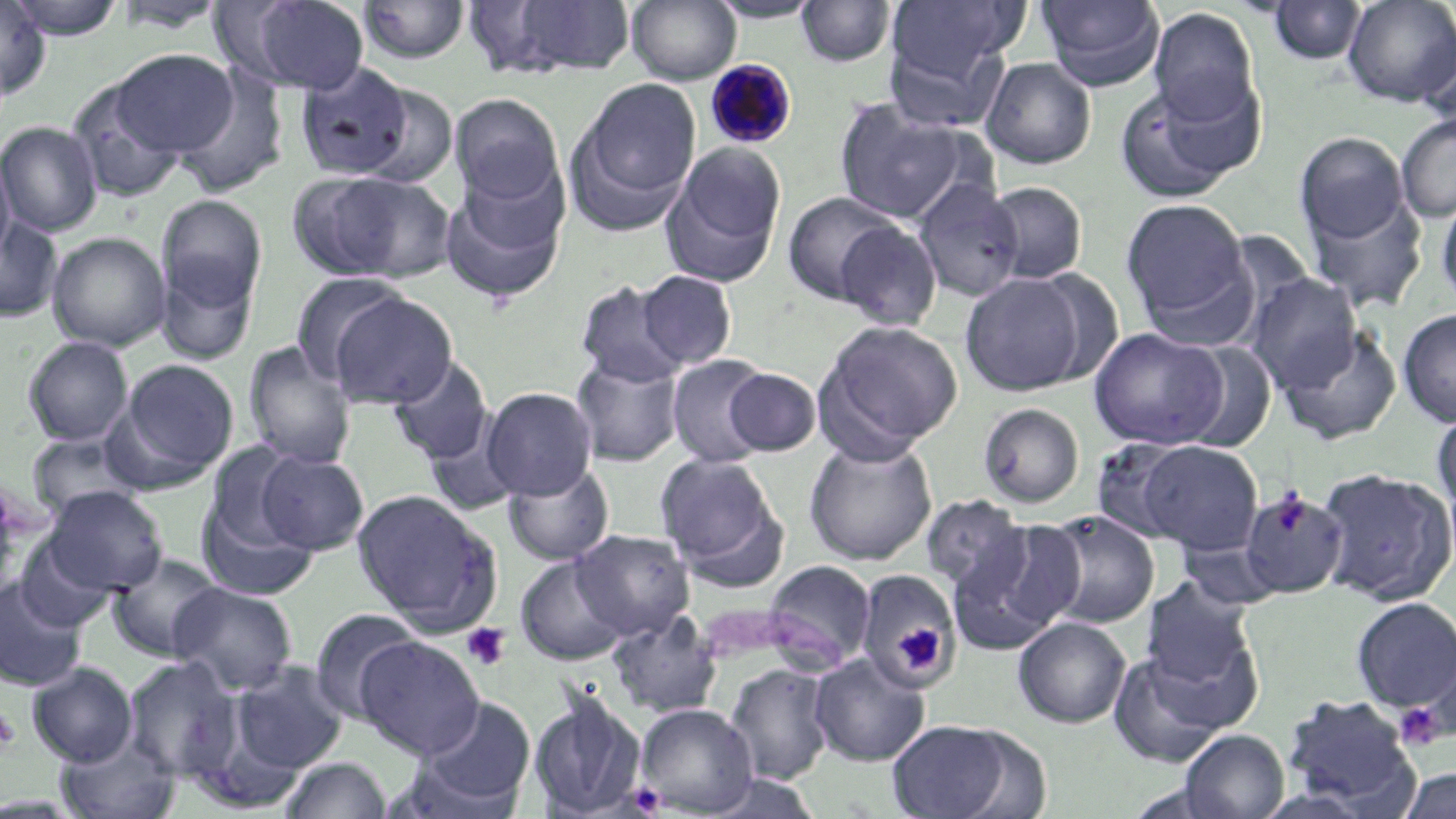

slide-level diagnosis = Plasmodium malariae
modality = light microscopy
Plasmodium malariae-infected red blood cell locations = approximate bounding boxes as named x1/y1/x2/y2 corners in pixels: (x1=705, y1=59, x2=798, y2=149)
magnification = 1000x
platelet locations = approximate bounding boxes as named x1/y1/x2/y2 corners in pixels: (x1=1271, y1=491, x2=1311, y2=535), (x1=461, y1=622, x2=511, y2=671), (x1=896, y1=623, x2=946, y2=674), (x1=1394, y1=703, x2=1446, y2=751), (x1=0, y1=709, x2=20, y2=752)
field of view = one of a larger specimen
image size = 1456×819 pixels
preparation = thin blood film
uninfected red blood cell locations = approximate bounding boxes as named x1/y1/x2/y2 corners in pixels: (x1=6, y1=0, x2=128, y2=39), (x1=232, y1=0, x2=370, y2=95), (x1=485, y1=0, x2=637, y2=78), (x1=627, y1=0, x2=741, y2=84), (x1=706, y1=0, x2=825, y2=23), (x1=1034, y1=0, x2=1166, y2=91), (x1=1342, y1=0, x2=1455, y2=107), (x1=0, y1=1, x2=50, y2=100), (x1=110, y1=1, x2=232, y2=34), (x1=357, y1=1, x2=471, y2=65), (x1=794, y1=1, x2=896, y2=68), (x1=885, y1=1, x2=1028, y2=84), (x1=1265, y1=1, x2=1368, y2=66), (x1=1147, y1=7, x2=1261, y2=126), (x1=1417, y1=28, x2=1455, y2=129), (x1=882, y1=31, x2=1010, y2=130), (x1=111, y1=49, x2=240, y2=157), (x1=980, y1=57, x2=1097, y2=169), (x1=295, y1=63, x2=414, y2=180), (x1=173, y1=67, x2=288, y2=197), (x1=570, y1=77, x2=702, y2=229), (x1=66, y1=78, x2=190, y2=204), (x1=1112, y1=79, x2=1257, y2=203), (x1=352, y1=83, x2=461, y2=189), (x1=449, y1=93, x2=564, y2=205), (x1=833, y1=100, x2=975, y2=225), (x1=1396, y1=114, x2=1456, y2=221), (x1=0, y1=121, x2=103, y2=236), (x1=1294, y1=131, x2=1410, y2=250), (x1=662, y1=144, x2=787, y2=285), (x1=0, y1=147, x2=16, y2=267), (x1=439, y1=168, x2=569, y2=303), (x1=300, y1=171, x2=455, y2=283), (x1=912, y1=179, x2=1024, y2=301), (x1=982, y1=181, x2=1089, y2=284), (x1=1302, y1=187, x2=1427, y2=313), (x1=1435, y1=190, x2=1456, y2=311), (x1=782, y1=191, x2=904, y2=306), (x1=157, y1=194, x2=267, y2=313), (x1=1121, y1=197, x2=1253, y2=329), (x1=0, y1=215, x2=63, y2=322), (x1=834, y1=220, x2=943, y2=331), (x1=47, y1=231, x2=171, y2=352), (x1=156, y1=257, x2=258, y2=365), (x1=636, y1=270, x2=738, y2=369), (x1=960, y1=271, x2=1092, y2=396), (x1=290, y1=272, x2=412, y2=381), (x1=1245, y1=274, x2=1363, y2=391), (x1=574, y1=280, x2=688, y2=387), (x1=327, y1=292, x2=457, y2=409), (x1=1397, y1=308, x2=1456, y2=426), (x1=814, y1=319, x2=964, y2=457), (x1=1089, y1=327, x2=1229, y2=450), (x1=1278, y1=328, x2=1402, y2=444), (x1=22, y1=336, x2=134, y2=446), (x1=243, y1=341, x2=356, y2=469), (x1=1179, y1=342, x2=1277, y2=453), (x1=571, y1=354, x2=684, y2=467), (x1=666, y1=354, x2=775, y2=468), (x1=388, y1=356, x2=494, y2=465), (x1=114, y1=357, x2=239, y2=483), (x1=723, y1=367, x2=823, y2=456), (x1=482, y1=387, x2=597, y2=500), (x1=977, y1=402, x2=1085, y2=508), (x1=1432, y1=408, x2=1456, y2=516), (x1=426, y1=423, x2=522, y2=517), (x1=27, y1=433, x2=143, y2=522), (x1=803, y1=437, x2=938, y2=565), (x1=1089, y1=437, x2=1202, y2=545), (x1=1137, y1=441, x2=1263, y2=555), (x1=200, y1=442, x2=310, y2=555), (x1=256, y1=450, x2=369, y2=555), (x1=655, y1=453, x2=785, y2=579), (x1=504, y1=464, x2=615, y2=565), (x1=1317, y1=468, x2=1455, y2=605), (x1=42, y1=486, x2=168, y2=596), (x1=352, y1=488, x2=503, y2=635), (x1=1239, y1=488, x2=1348, y2=599), (x1=196, y1=492, x2=319, y2=602), (x1=919, y1=494, x2=1033, y2=605), (x1=1043, y1=510, x2=1159, y2=628), (x1=948, y1=519, x2=1084, y2=651), (x1=571, y1=528, x2=696, y2=640), (x1=12, y1=536, x2=120, y2=632), (x1=105, y1=552, x2=226, y2=663), (x1=515, y1=554, x2=629, y2=666), (x1=763, y1=560, x2=877, y2=671), (x1=856, y1=569, x2=958, y2=687), (x1=0, y1=577, x2=89, y2=692), (x1=1140, y1=580, x2=1256, y2=690), (x1=169, y1=582, x2=299, y2=695), (x1=1350, y1=596, x2=1456, y2=715), (x1=309, y1=608, x2=423, y2=723), (x1=607, y1=610, x2=723, y2=719), (x1=1013, y1=617, x2=1131, y2=728), (x1=354, y1=635, x2=485, y2=759), (x1=1108, y1=651, x2=1232, y2=766), (x1=809, y1=653, x2=930, y2=766), (x1=122, y1=657, x2=242, y2=781), (x1=27, y1=662, x2=138, y2=766), (x1=229, y1=662, x2=349, y2=774), (x1=724, y1=663, x2=835, y2=785), (x1=189, y1=685, x2=318, y2=806), (x1=528, y1=691, x2=647, y2=819), (x1=1281, y1=695, x2=1419, y2=812), (x1=413, y1=696, x2=537, y2=812), (x1=635, y1=703, x2=759, y2=816), (x1=885, y1=718, x2=1026, y2=819), (x1=1178, y1=729, x2=1289, y2=819), (x1=55, y1=733, x2=180, y2=819), (x1=278, y1=756, x2=392, y2=818), (x1=1399, y1=768, x2=1456, y2=818)
stain = May-Grünwald-Giemsa